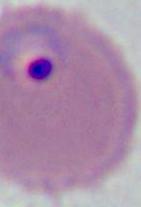
modality = micrograph
magnification = 400x or 1000x
identification = Plasmodium